Assess the morphology of the red blood cells.
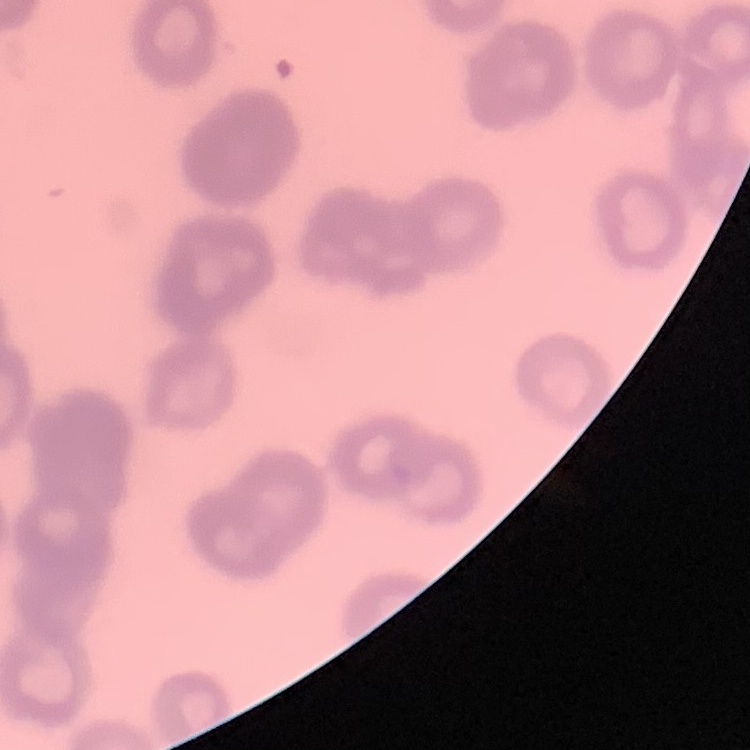

They show rouleaux formation.

preparation = thin peripheral smear
image type = one tile cut from a larger photomicrograph
stain = Field's or Giemsa